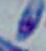
Summary:
  - Modality: photomicrograph
  - Identification: Toxoplasma gondii
  - Magnification: 1000x